Classify this cell by malaria status.
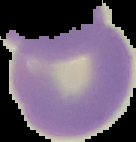

Uninfected.

From a thin blood film. Segmented cell region on a black background. Image is 136×142 pixels.